Report the malaria status.
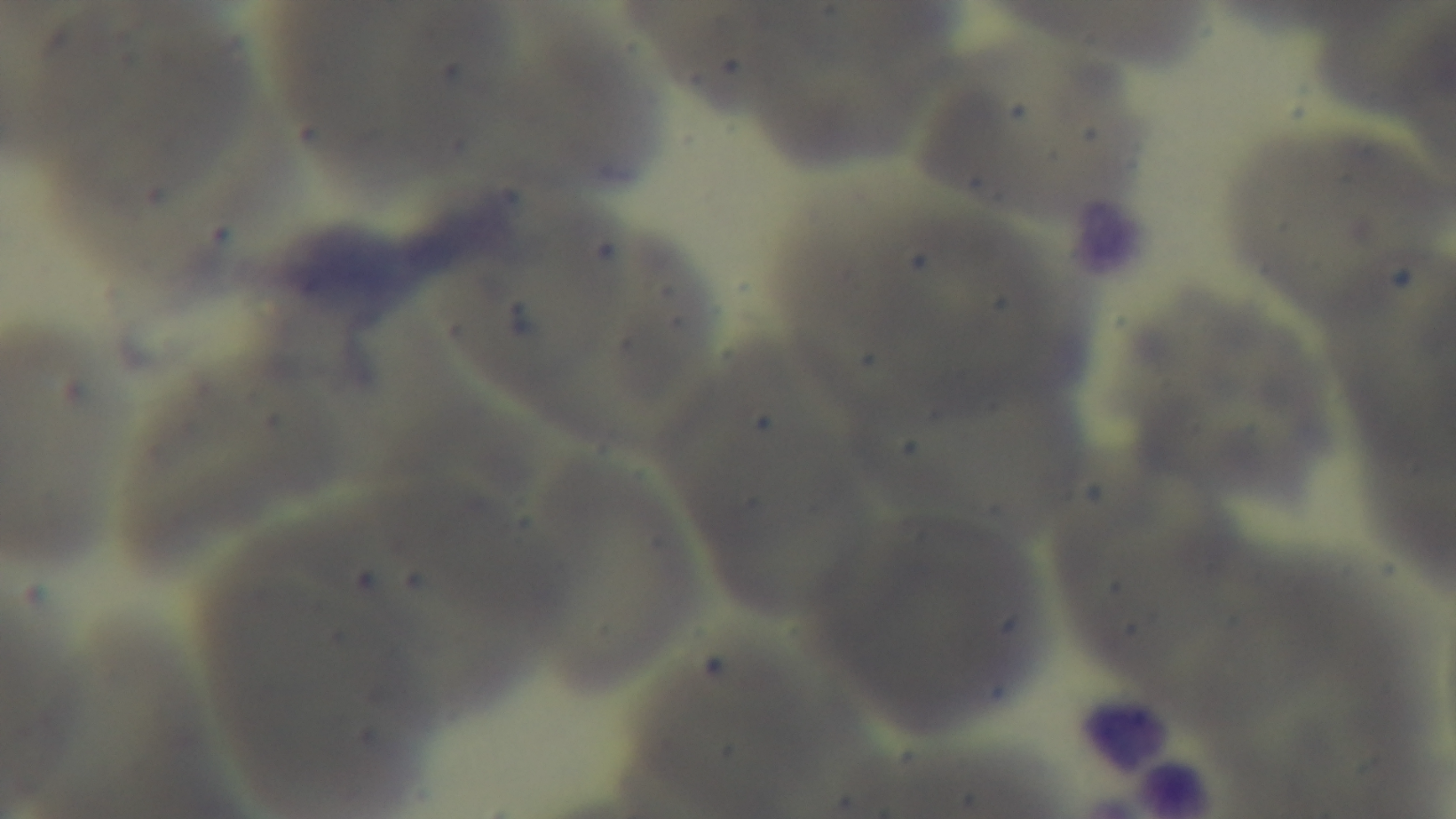

Uninfected.

Summary:
  - Capture: mounted 4K digital camera
  - Objective: 100x oil immersion
  - Field of view: single
  - Preparation: thin smear
  - Stain: Giemsa
  - Modality: light microscopy